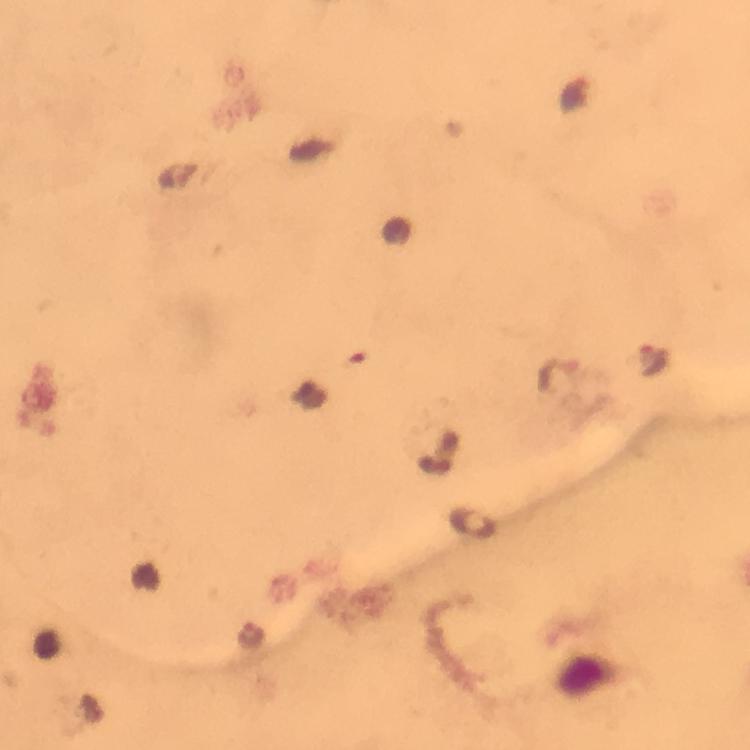
Approximate object centers, in pixels from the top-left corner. Malaria parasite locations: (x=652, y=360), (x=251, y=634). Image is 750×750 pixels. Thick smear. Immersion oil applied. 100x magnification. Giemsa stain. A crop from one field of view. Photographed through the microscope with a smartphone camera. From a malaria diagnostic workup.